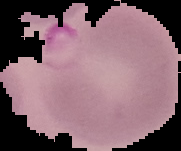
preparation: thin blood film
malaria_status: parasitized
image_type: segmented cell region on a black background
image_size: 181×151 pixels